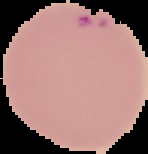

From a thin blood film. Image is 148×154 pixels. Malaria status: parasitized. Segmented cell region on a black background.